Describe the morphology of the red blood cells.
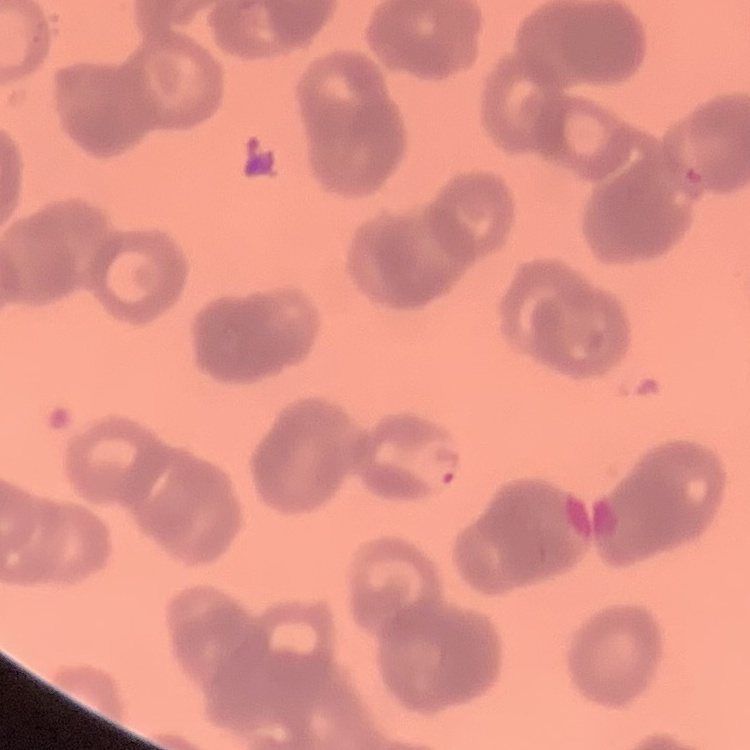
Rouleaux formation.

Summary:
  - Preparation: thin blood smear
  - Stain: Field's or Giemsa
  - Image type: one tile cut from a larger photomicrograph